Assess the morphology of the red blood cells.
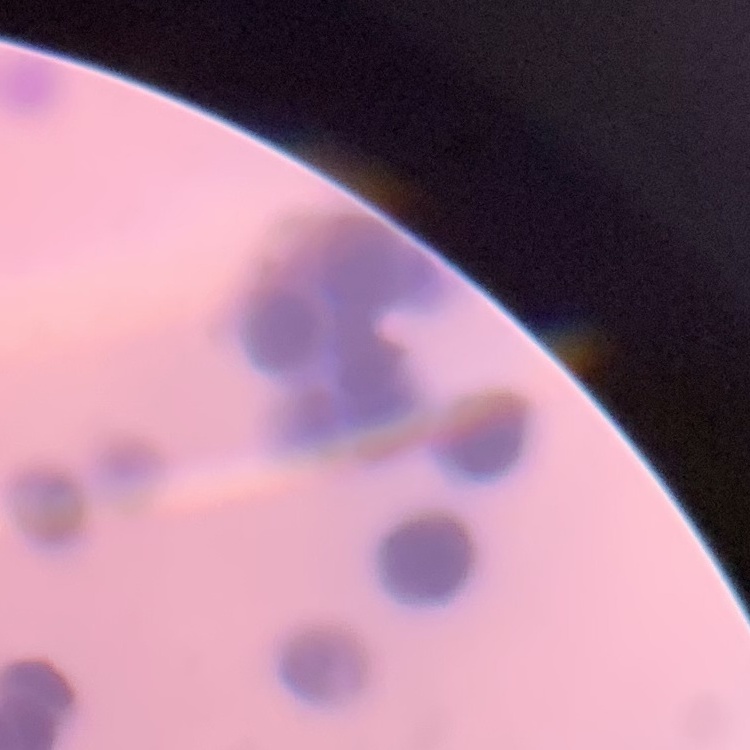
They show rouleaux formation.

preparation: thin peripheral smear
stain: Field's or Giemsa
image_type: square crop of a larger photomicrograph